Name the parasite shown.
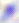

This is Toxoplasma gondii.

400x magnification. Photomicrograph.